Locate every Plasmodium parasite.
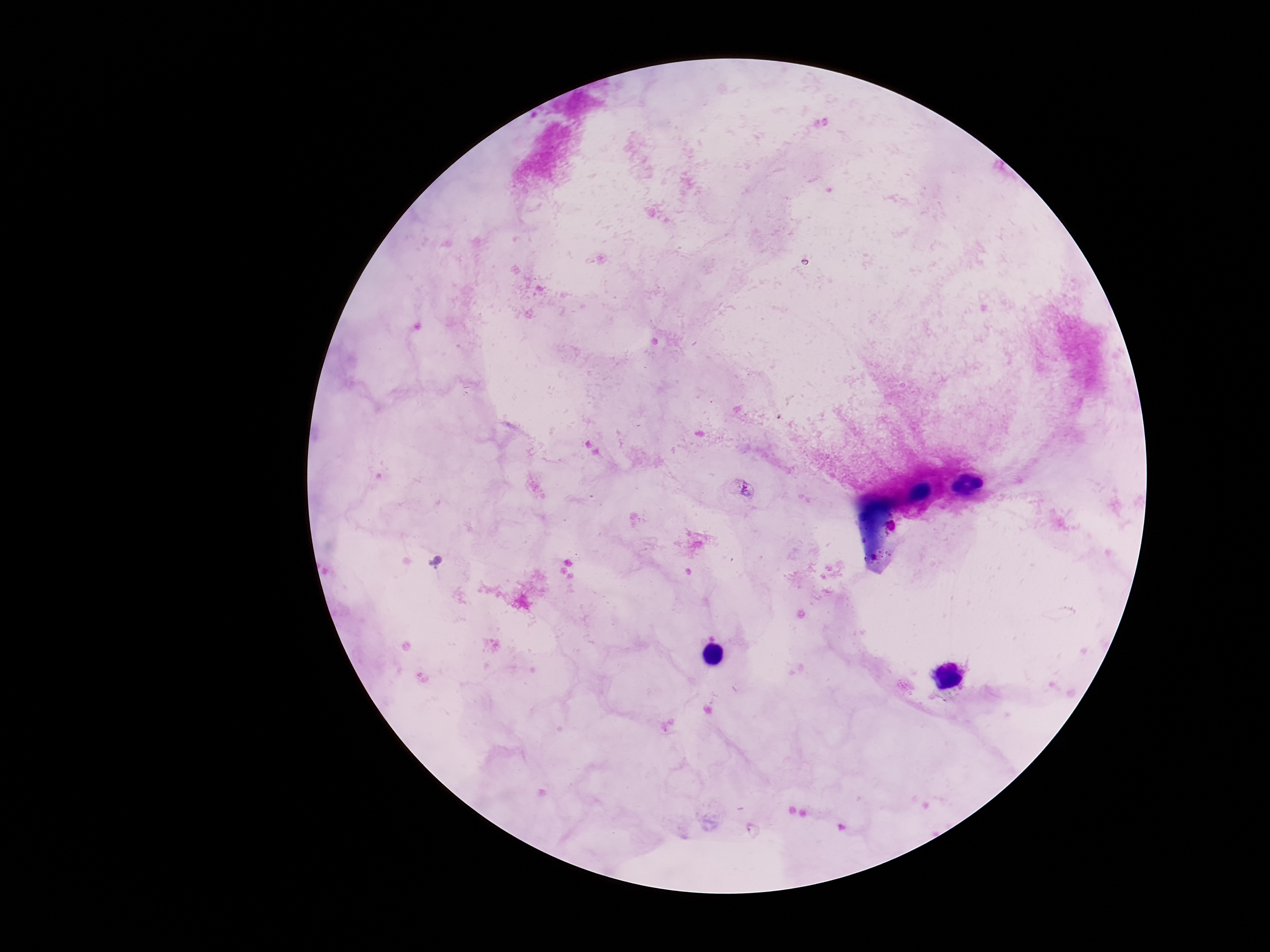

Approximate object centers, in pixels from the top-left corner.
Plasmodium parasites: (x=746, y=489).

Image is 1270×952 pixels. Thick peripheral-blood smear. Giemsa-stained preparation. 100x magnification. Patient malaria status: infected. Single field of view. Smartphone photograph taken through the microscope eyepiece.